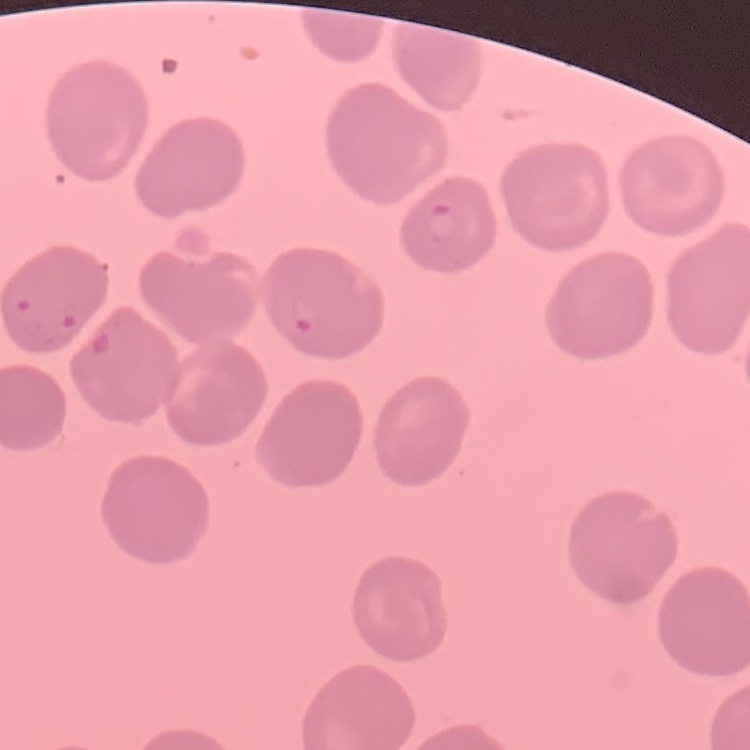

The red blood cells show no rouleaux formation. Square crop of a larger photomicrograph. Thin blood smear. Field's or Giemsa stain.